Evaluate for Plasmodium parasites.
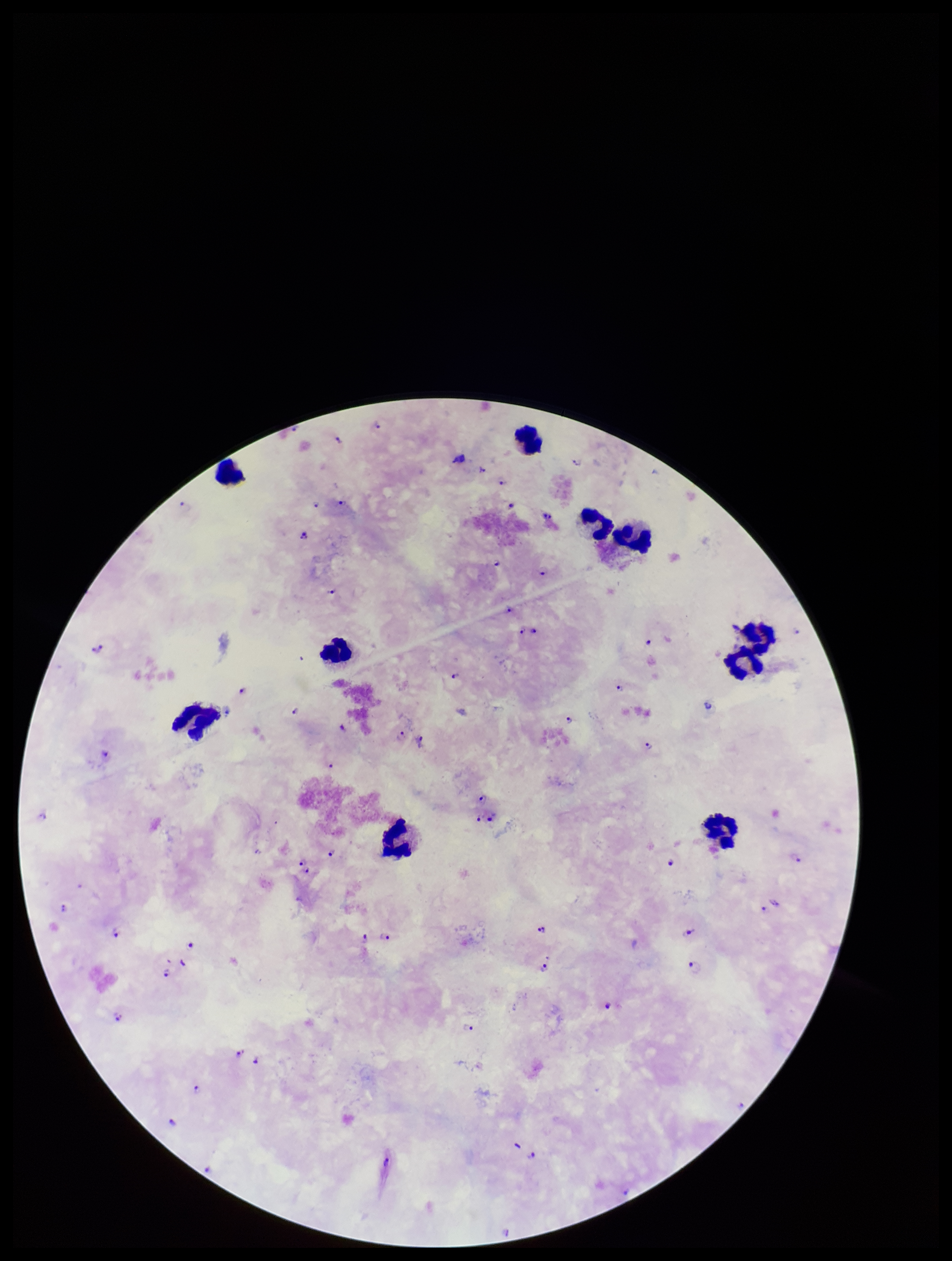

Seen.

stain = Giemsa
capture = smartphone photograph through the microscope eyepiece
field of view = single
image size = 952×1261 pixels
species reported for this patient = Plasmodium falciparum
parasite count = 62
leukocyte count = 10
patient malaria status = infected
preparation = thick blood smear